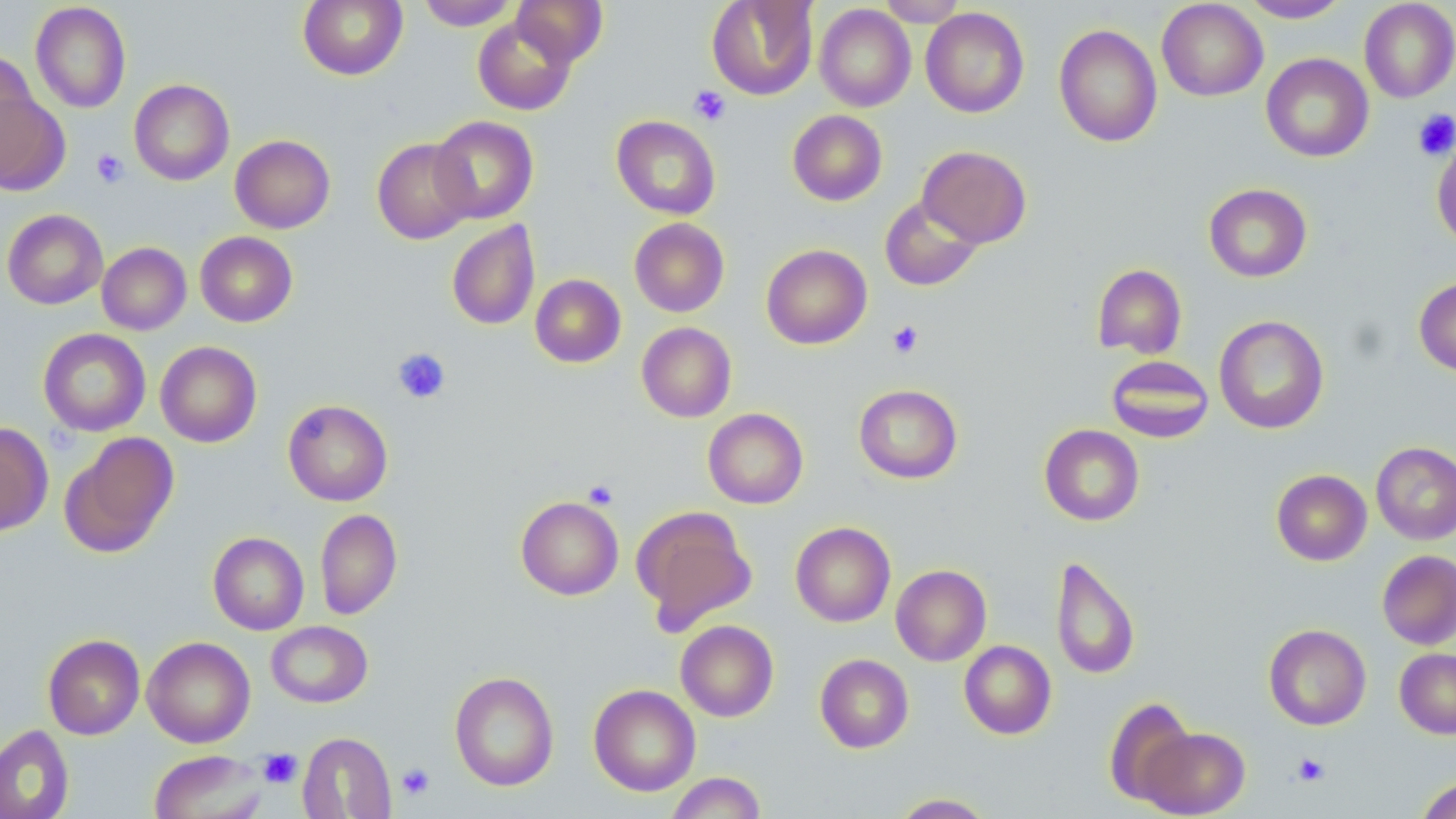

{
  "slide_level_diagnosis": "no evidence of blood parasites",
  "preparation": "thin blood smear",
  "platelet_locations": "approximate bounding boxes as named x1/y1/x2/y2 corners in pixels: (x1=689, y1=85, x2=731, y2=126), (x1=1412, y1=109, x2=1456, y2=160), (x1=91, y1=148, x2=129, y2=188), (x1=887, y1=320, x2=923, y2=358), (x1=392, y1=348, x2=451, y2=403), (x1=582, y1=479, x2=619, y2=509), (x1=258, y1=748, x2=303, y2=788), (x1=1292, y1=753, x2=1329, y2=786), (x1=396, y1=763, x2=435, y2=800)",
  "magnification": "1000x",
  "stain": "May-Grünwald-Giemsa",
  "uninfected_red_blood_cell_locations": "approximate bounding boxes as named x1/y1/x2/y2 corners in pixels: (x1=297, y1=0, x2=408, y2=81), (x1=417, y1=0, x2=521, y2=30), (x1=512, y1=0, x2=608, y2=66), (x1=706, y1=0, x2=818, y2=100), (x1=877, y1=0, x2=968, y2=26), (x1=1238, y1=0, x2=1352, y2=23), (x1=1156, y1=1, x2=1268, y2=101), (x1=1359, y1=1, x2=1456, y2=103), (x1=30, y1=2, x2=131, y2=113), (x1=814, y1=4, x2=916, y2=112), (x1=920, y1=7, x2=1030, y2=118), (x1=472, y1=16, x2=576, y2=115), (x1=1053, y1=23, x2=1163, y2=147), (x1=1, y1=51, x2=39, y2=162), (x1=1261, y1=53, x2=1374, y2=162), (x1=129, y1=79, x2=234, y2=185), (x1=0, y1=88, x2=69, y2=196), (x1=787, y1=110, x2=887, y2=206), (x1=611, y1=115, x2=721, y2=219), (x1=429, y1=116, x2=539, y2=224), (x1=230, y1=134, x2=336, y2=233), (x1=372, y1=137, x2=476, y2=244), (x1=1431, y1=137, x2=1456, y2=247), (x1=917, y1=145, x2=1032, y2=248), (x1=1203, y1=183, x2=1312, y2=282), (x1=879, y1=196, x2=983, y2=291), (x1=2, y1=209, x2=108, y2=309), (x1=629, y1=218, x2=729, y2=317), (x1=447, y1=220, x2=540, y2=330), (x1=195, y1=231, x2=298, y2=327), (x1=97, y1=242, x2=191, y2=335), (x1=761, y1=244, x2=872, y2=349), (x1=1092, y1=263, x2=1187, y2=359), (x1=530, y1=274, x2=626, y2=368), (x1=1413, y1=276, x2=1456, y2=376), (x1=1214, y1=315, x2=1329, y2=434), (x1=636, y1=322, x2=737, y2=422), (x1=38, y1=328, x2=151, y2=436), (x1=155, y1=341, x2=262, y2=448), (x1=1106, y1=355, x2=1214, y2=443), (x1=853, y1=384, x2=963, y2=484), (x1=283, y1=400, x2=393, y2=506), (x1=703, y1=408, x2=809, y2=509), (x1=0, y1=423, x2=53, y2=536), (x1=1039, y1=424, x2=1144, y2=526), (x1=59, y1=432, x2=179, y2=557), (x1=1371, y1=441, x2=1456, y2=545), (x1=1271, y1=469, x2=1372, y2=565), (x1=516, y1=496, x2=624, y2=600), (x1=632, y1=505, x2=757, y2=634), (x1=315, y1=508, x2=402, y2=619), (x1=790, y1=522, x2=896, y2=627), (x1=208, y1=532, x2=309, y2=635), (x1=1376, y1=550, x2=1456, y2=650), (x1=1050, y1=555, x2=1140, y2=680), (x1=891, y1=564, x2=991, y2=666), (x1=675, y1=620, x2=779, y2=722), (x1=266, y1=621, x2=373, y2=708), (x1=1263, y1=624, x2=1371, y2=730), (x1=42, y1=634, x2=145, y2=740), (x1=142, y1=636, x2=256, y2=748), (x1=959, y1=640, x2=1056, y2=739), (x1=1394, y1=648, x2=1456, y2=738), (x1=815, y1=653, x2=914, y2=753), (x1=449, y1=671, x2=559, y2=791), (x1=589, y1=684, x2=701, y2=796), (x1=1103, y1=696, x2=1195, y2=805), (x1=0, y1=724, x2=74, y2=819), (x1=1139, y1=726, x2=1250, y2=817), (x1=297, y1=732, x2=396, y2=818), (x1=149, y1=750, x2=268, y2=819), (x1=665, y1=772, x2=767, y2=818), (x1=1415, y1=776, x2=1456, y2=819), (x1=889, y1=793, x2=997, y2=818)",
  "field_of_view": "one of a larger specimen",
  "modality": "light microscopy",
  "image_size": "1456×819 pixels"
}